Identify the parasite.
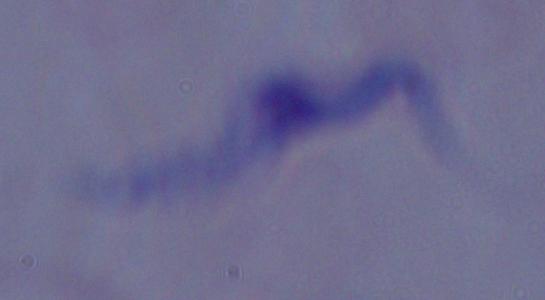

This is a trypanosome.

Summary:
  - Modality: photomicrograph
  - Magnification: 1000x